Classify this cell by malaria status.
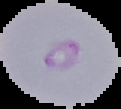

It is parasitized.

preparation = thin blood smear
image size = 121×109 pixels
image type = cell region segmented out of the field of view; surrounding area masked to black